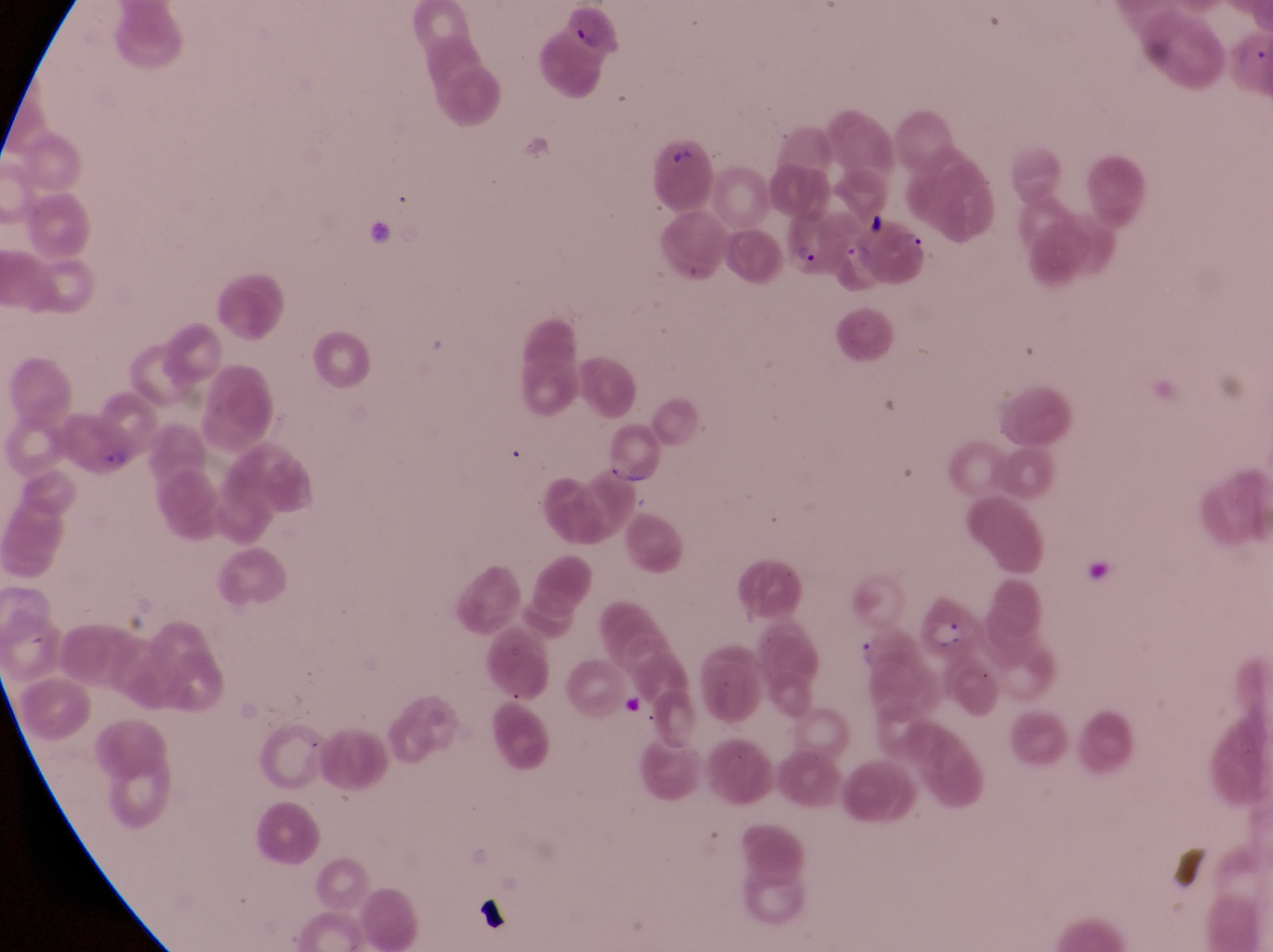
Approximate bounding boxes as {left, top, right, bottom} in pixels. Parasitised red blood cell locations: {782, 210, 847, 272}, {870, 221, 933, 284}, {62, 412, 142, 487}, {604, 431, 666, 488}, {919, 589, 986, 663}. Trophozoite locations: {849, 629, 881, 674}. Artifact (platelet-like body, stain precipitate, or debris) locations: {859, 207, 889, 230}. Image is 1273×952 pixels. Collected in Uganda. Thin blood film. One field of view. Magnification of 1000x. Photographed through the eyepiece of an Olympus CX-23 microscope with a smartphone camera.